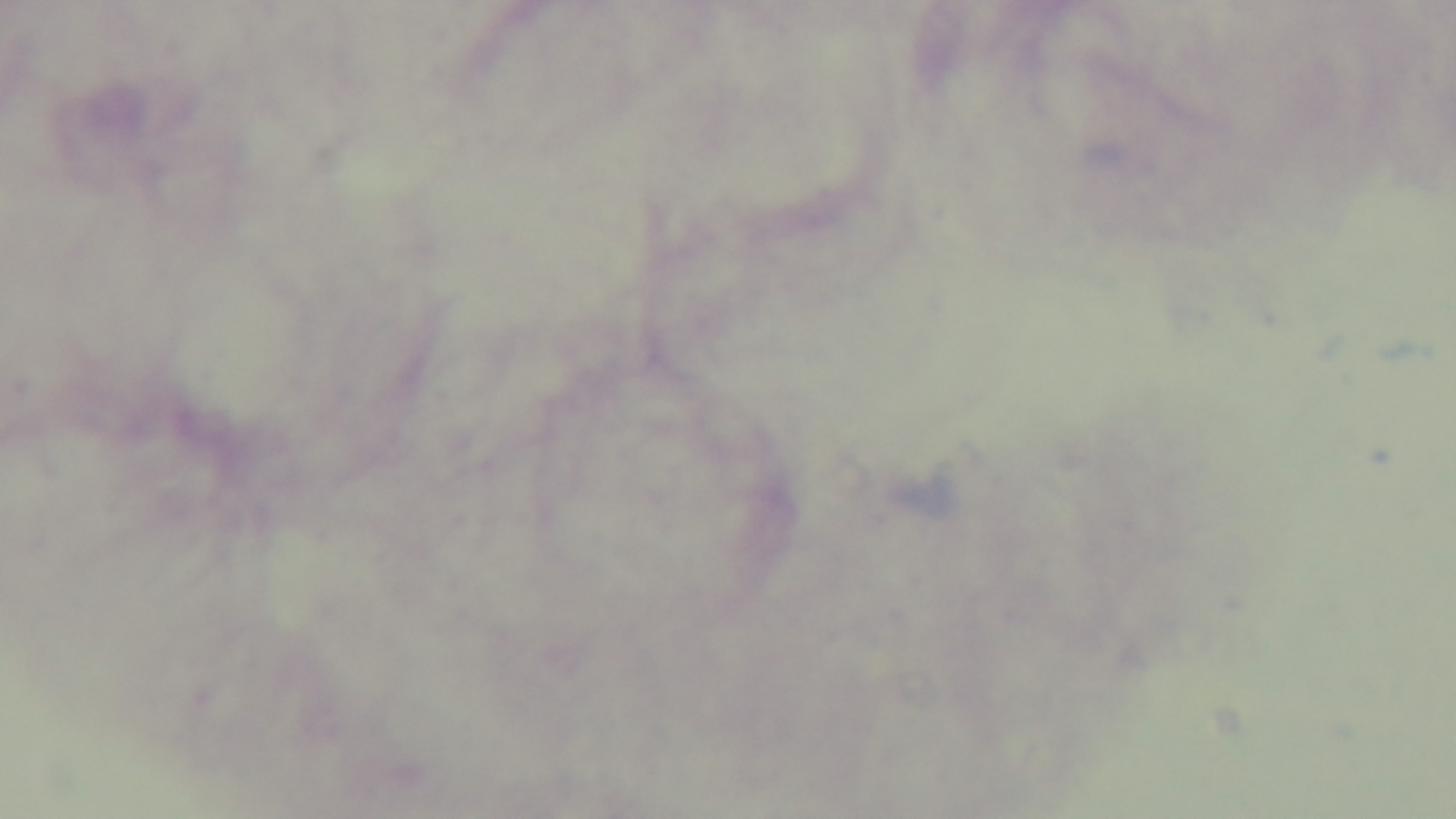

field of view = single
preparation = thick blood film
stain = Giemsa
modality = light microscopy
malaria status = uninfected
capture = mounted 4K digital camera
objective = 100x oil immersion